Classify this cell by malaria status.
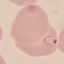
It is parasitized.

Summary:
  - Capture: smartphone camera at the microscope eyepiece
  - Image type: cell patch, automatically extracted from a larger field of view and resized to 64 × 64 pixels
  - Preparation: thin blood smear
  - Stain: Giemsa